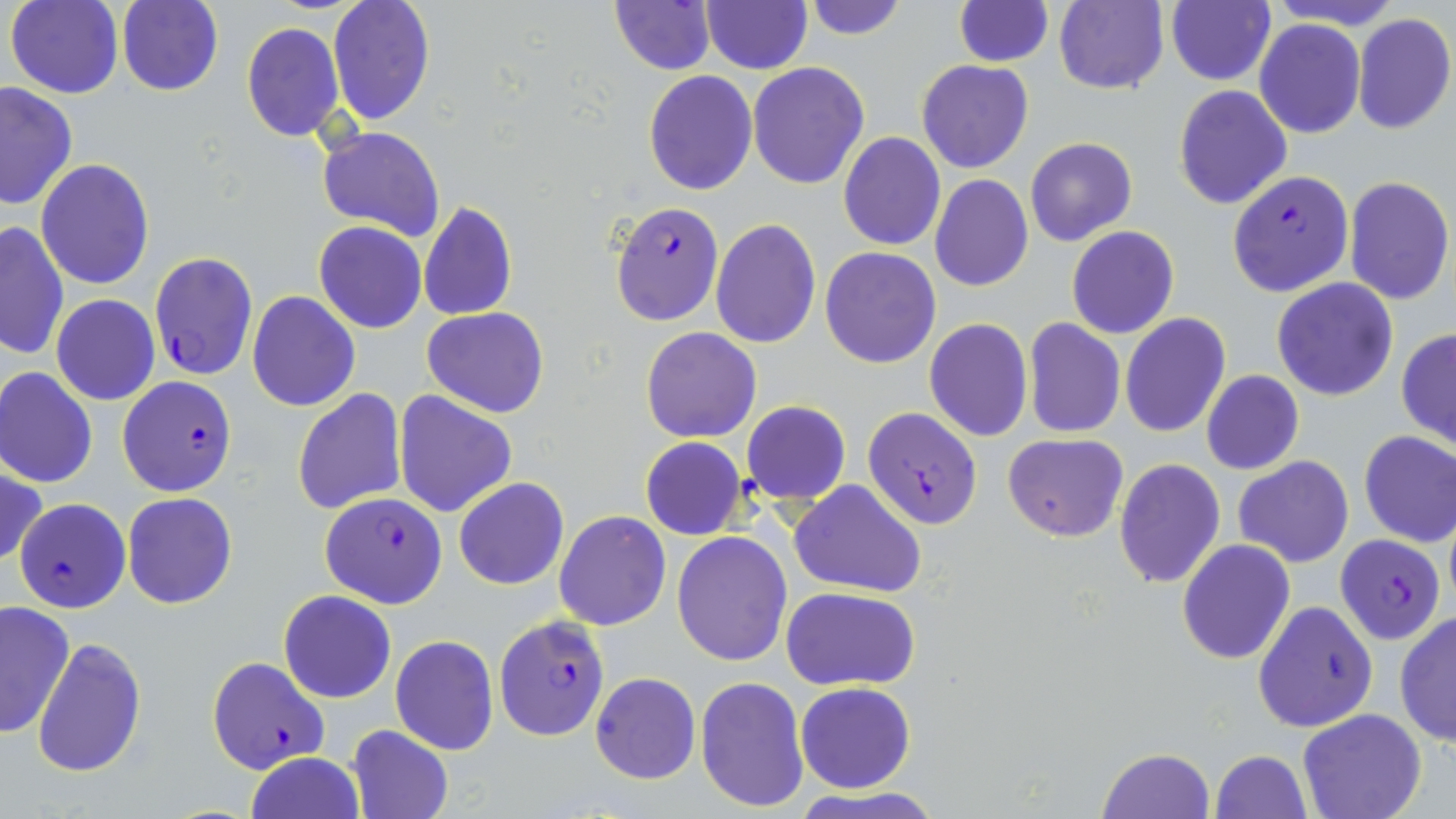

Summary:
  - Coordinate format: approximate bounding boxes as (x1, y1, x2, y2) in pixels
  - Plasmodium falciparum-infected red blood cell locations: (1228, 170, 1354, 297), (609, 201, 723, 325), (149, 252, 258, 382), (118, 375, 238, 497), (862, 409, 981, 529), (319, 491, 447, 610), (12, 498, 130, 612), (1334, 536, 1446, 644), (495, 616, 611, 739), (206, 656, 329, 773)
  - Uninfected red blood cell locations: (326, 0, 436, 127), (608, 0, 719, 75), (802, 0, 907, 40), (1051, 0, 1169, 93), (6, 1, 124, 99), (952, 1, 1053, 66), (116, 2, 223, 96), (1165, 2, 1276, 86), (701, 3, 811, 74), (1352, 13, 1456, 135), (1254, 19, 1365, 139), (239, 21, 345, 141), (917, 60, 1033, 173), (747, 61, 869, 189), (643, 71, 758, 194), (1, 81, 78, 212), (1173, 84, 1292, 209), (318, 127, 443, 242), (838, 131, 945, 250), (1025, 137, 1137, 247), (35, 160, 154, 290), (929, 175, 1033, 291), (1342, 175, 1454, 306), (419, 200, 517, 321), (710, 218, 822, 349), (0, 220, 70, 360), (314, 222, 427, 333), (1066, 225, 1180, 340), (280, 245, 400, 380), (820, 246, 941, 367), (1272, 277, 1399, 401), (246, 291, 360, 411), (51, 295, 160, 405), (422, 307, 548, 418), (1120, 312, 1231, 439), (924, 318, 1033, 440), (1023, 318, 1125, 437), (640, 326, 761, 443), (1396, 327, 1456, 452), (0, 367, 97, 487), (1201, 369, 1304, 476), (293, 388, 407, 514), (393, 390, 518, 518), (740, 400, 852, 504), (1358, 430, 1456, 548), (1002, 433, 1129, 541), (640, 437, 746, 540), (1234, 456, 1354, 567), (1113, 458, 1226, 589), (0, 465, 46, 569), (454, 477, 569, 590), (790, 479, 928, 599), (121, 493, 237, 609), (554, 510, 671, 629), (672, 531, 792, 666), (1176, 539, 1295, 665), (782, 587, 920, 691), (278, 590, 396, 703), (1252, 599, 1379, 733), (0, 601, 77, 740), (1394, 610, 1456, 746), (391, 635, 499, 755), (32, 637, 147, 778), (589, 671, 701, 785), (695, 675, 808, 811), (795, 682, 916, 793), (1298, 710, 1425, 819), (346, 724, 454, 819), (1099, 747, 1214, 818), (1210, 749, 1311, 819), (245, 751, 365, 819)
  - Slide-level diagnosis: Plasmodium falciparum
  - Stain: May-Grünwald-Giemsa
  - Field of view: one of a larger specimen
  - Magnification: 1000x
  - Preparation: thin blood film
  - Modality: light microscopy
  - Image size: 1456×819 pixels